Give the position of every malaria parasite.
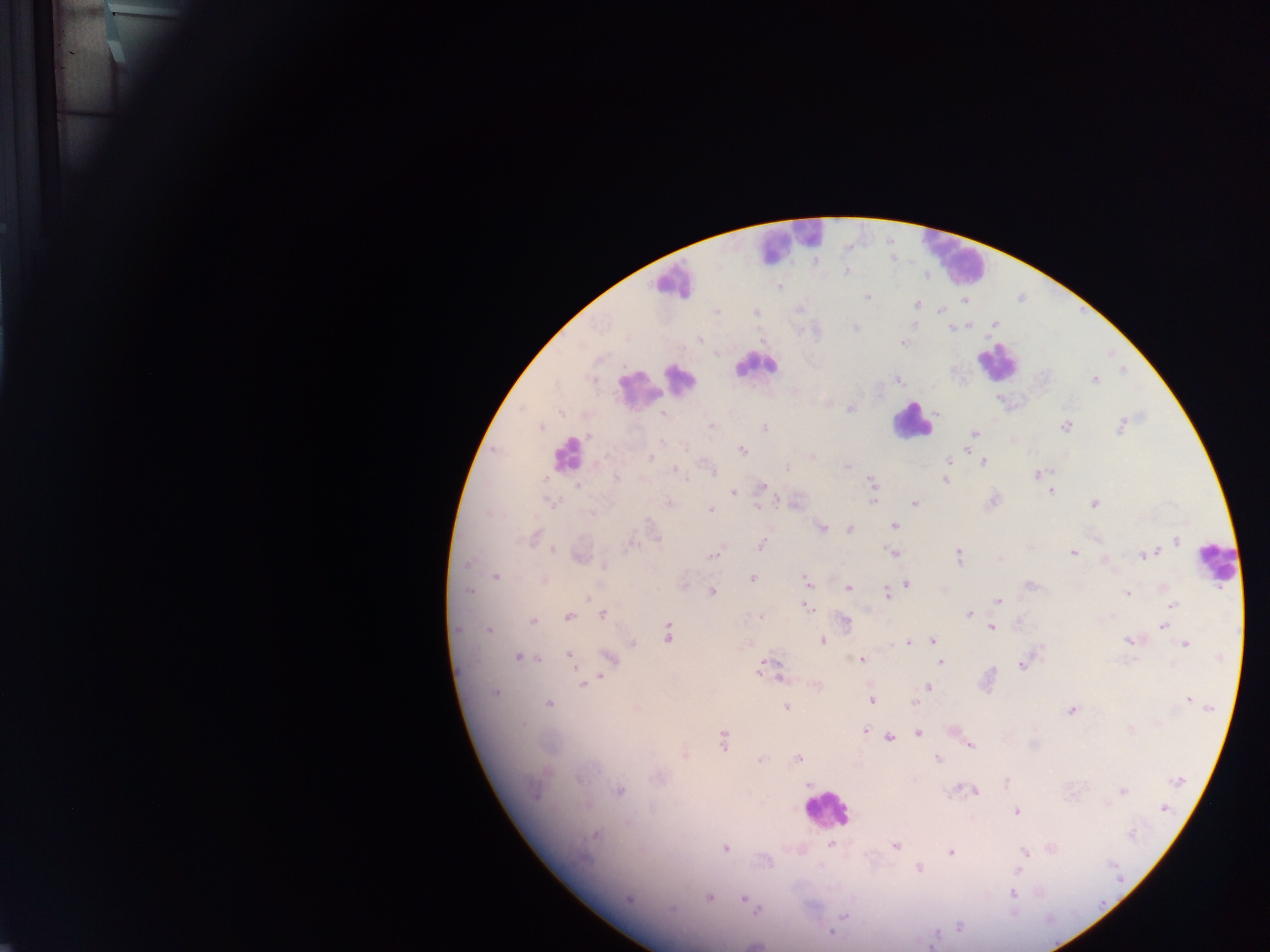
Approximate centers as [x, y] in pixels.
Malaria parasites: [892, 261], [845, 273], [781, 288], [685, 293], [866, 297], [964, 303], [916, 305], [939, 310], [994, 323], [973, 325], [855, 328], [949, 329], [955, 329], [700, 338], [902, 344], [1123, 370], [622, 377], [898, 379], [1095, 380], [850, 408], [560, 410], [664, 415], [1123, 420], [710, 425], [541, 426], [1067, 426], [765, 427], [1120, 428], [975, 433], [590, 434], [662, 442], [743, 450], [652, 457], [946, 462], [982, 463], [847, 465], [788, 468], [675, 469], [710, 470], [1037, 474], [948, 475], [615, 478], [544, 479], [946, 480], [870, 482], [763, 487], [576, 490], [1051, 490], [734, 494], [873, 497], [544, 501], [549, 501], [778, 501], [993, 501], [912, 502], [668, 503], [1093, 504], [757, 505], [710, 510], [487, 513], [895, 527], [821, 529], [849, 529], [536, 536], [657, 540], [1178, 541], [761, 545], [623, 547], [553, 550], [627, 550], [891, 552], [1072, 552], [714, 554], [958, 555], [1143, 555], [999, 557], [465, 565], [603, 569], [495, 577], [752, 578], [544, 581], [805, 581], [907, 582], [1029, 585], [848, 589], [712, 591], [469, 592], [887, 593], [1128, 593], [589, 599], [998, 601], [1172, 605], [806, 607], [968, 614], [603, 615], [568, 616], [761, 616], [757, 617], [843, 621], [533, 622], [1163, 626], [990, 627], [459, 630], [489, 630], [668, 635], [932, 641], [1126, 641], [821, 642], [909, 643], [633, 644], [1185, 644], [567, 655], [518, 657], [861, 660], [540, 661], [941, 662], [768, 663], [1021, 665], [760, 669], [992, 670], [778, 677], [600, 678], [782, 681], [589, 682], [582, 686], [930, 686], [494, 694], [872, 701], [1187, 701], [913, 703], [549, 704], [1209, 706], [786, 708], [1070, 711], [866, 729], [1131, 730], [918, 733], [890, 738], [723, 741], [972, 746], [685, 755], [798, 758], [759, 759], [939, 759], [1179, 781], [807, 784], [620, 790], [951, 790], [976, 790], [1123, 790], [536, 793], [1107, 806], [1165, 810], [1016, 813], [595, 835], [832, 845], [895, 846], [724, 849], [1051, 849], [949, 851], [1024, 852], [918, 866], [1018, 871], [1040, 892], [1013, 894], [630, 898], [709, 898], [742, 899], [669, 909], [757, 911], [843, 915], [959, 925], [829, 932].

Leukocyte locations: [792, 234], [957, 257], [672, 275], [1001, 363], [753, 365], [685, 383], [639, 391], [913, 424], [572, 457], [828, 813]. Single field of view. Mobile-phone photograph taken through the microscope. Thick blood film. Image is 1270×952 pixels. Collected in Ghana.